Locate every blood parasite and identify its species.
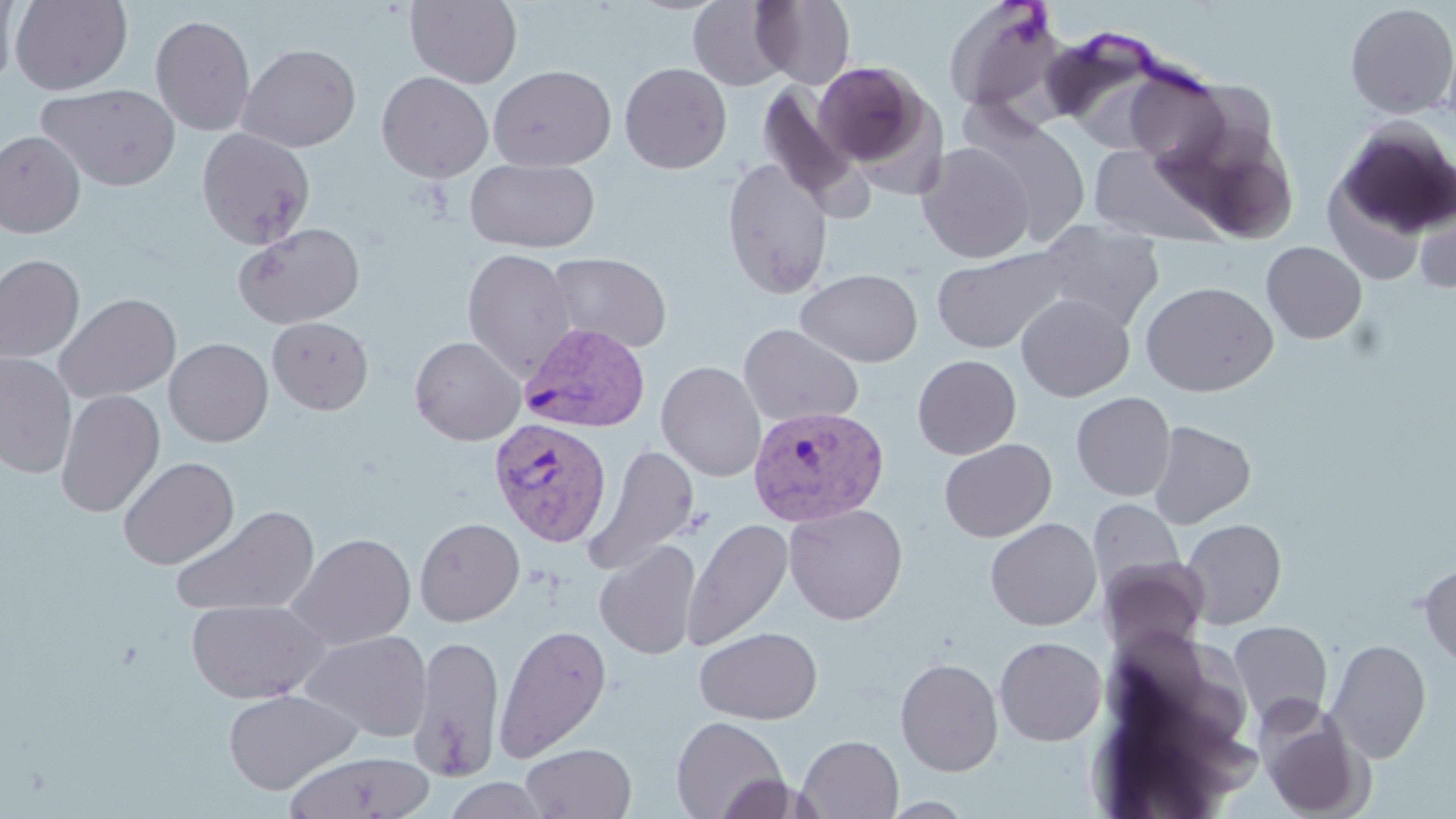
Approximate bounding boxes as [x1, y1, x2, y2] in pixels.
Plasmodium vivax-infected red blood cells: [518, 321, 652, 434], [748, 404, 889, 527], [489, 416, 613, 546].
No Plasmodium falciparum, Plasmodium ovale, Plasmodium malariae, Babesia divergens, or Trypanosoma brucei observed.

slide_level_diagnosis: Plasmodium vivax
image_size: 1456×819 pixels
magnification: 1000x
field_of_view: one of a larger specimen
preparation: thin blood film
stain: May-Grünwald-Giemsa
modality: light microscopy
uninfected_red_blood_cell_locations: 'approximate bounding boxes as [x1, y1, x2, y2] in pixels: [0, 0, 18, 92], [10, 0, 132, 94], [405, 0, 523, 88], [689, 0, 791, 91], [752, 0, 856, 89], [943, 0, 1068, 118], [1344, 2, 1456, 119], [150, 15, 255, 136], [238, 43, 361, 152], [812, 60, 932, 171], [620, 62, 732, 173], [488, 64, 616, 172], [1121, 70, 1232, 170], [376, 71, 493, 183], [756, 82, 861, 206], [38, 83, 181, 191], [965, 110, 1091, 247], [1330, 119, 1455, 245], [1165, 126, 1301, 243], [196, 128, 316, 249], [0, 130, 85, 237], [917, 142, 1035, 263], [1087, 143, 1223, 245], [465, 157, 600, 253], [721, 157, 833, 298], [1414, 190, 1455, 296], [1037, 218, 1164, 332], [233, 222, 365, 329], [1261, 241, 1367, 344], [932, 246, 1073, 354], [462, 248, 579, 382], [545, 252, 672, 354], [0, 254, 85, 364], [796, 268, 922, 367], [1141, 280, 1278, 396], [53, 292, 181, 404], [1015, 293, 1134, 401], [267, 316, 373, 415], [738, 324, 864, 427], [409, 336, 525, 446], [164, 337, 273, 446], [0, 352, 77, 478], [913, 354, 1021, 459], [657, 360, 767, 482], [55, 389, 165, 518], [1071, 391, 1176, 501], [1148, 420, 1256, 529], [939, 438, 1057, 542], [583, 444, 701, 576], [118, 457, 239, 570], [1088, 499, 1185, 602], [784, 503, 908, 625], [170, 505, 320, 618], [415, 517, 525, 626], [683, 517, 792, 651], [985, 517, 1102, 631], [1180, 518, 1287, 629], [286, 532, 416, 650], [595, 540, 701, 660], [1099, 557, 1210, 658], [1417, 559, 1456, 671], [185, 598, 329, 703], [1228, 620, 1333, 728], [494, 623, 611, 763], [694, 626, 823, 724], [684, 628, 803, 818], [301, 630, 433, 742], [408, 635, 505, 782], [993, 636, 1107, 746], [1325, 639, 1432, 763], [895, 657, 1004, 777], [223, 688, 362, 795], [1257, 706, 1370, 819], [670, 715, 789, 819], [797, 735, 903, 818], [521, 742, 636, 818], [284, 750, 436, 818], [714, 774, 817, 818], [441, 776, 552, 819]'